Identify the parasite.
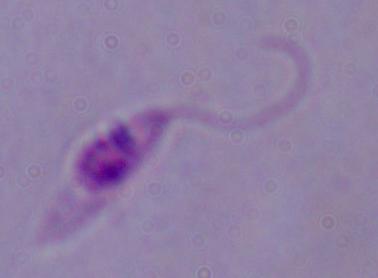

This is Leishmania.

Summary:
  - Modality: micrograph
  - Magnification: 1000x